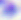

Summary:
  - Magnification: 400x
  - Modality: photomicrograph
  - Identification: Toxoplasma gondii